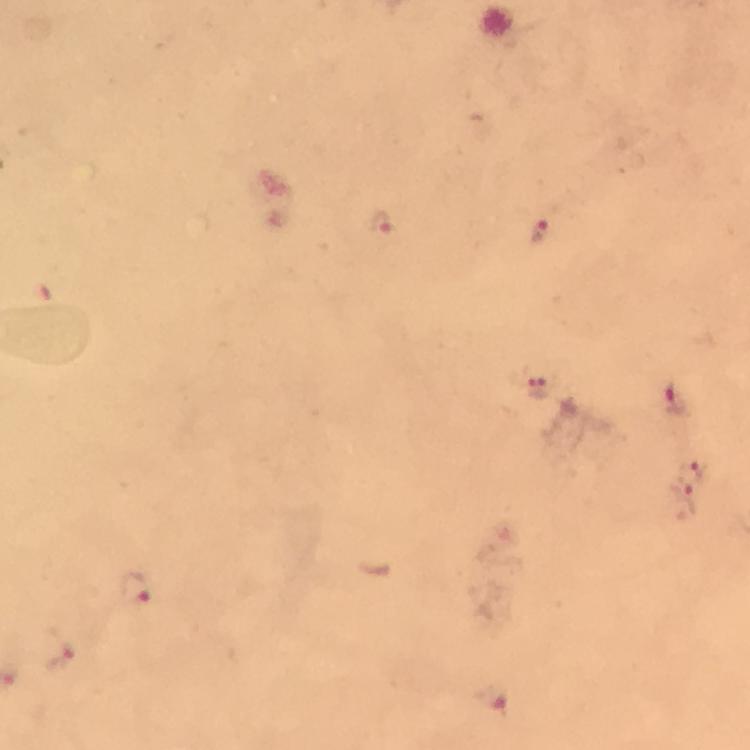
Approximate centers as {x, y} in pixels. Malaria parasite locations: {381, 222}, {540, 231}, {538, 390}, {675, 403}, {691, 466}, {683, 494}, {136, 590}, {58, 649}, {490, 700}. Giemsa-stained preparation. Image is 750×750 pixels. Thick smear. Cropped region of a single field of view. Smartphone photograph taken through a microscope. At 100x magnification. From a malaria diagnostic workup. Immersion oil was used.